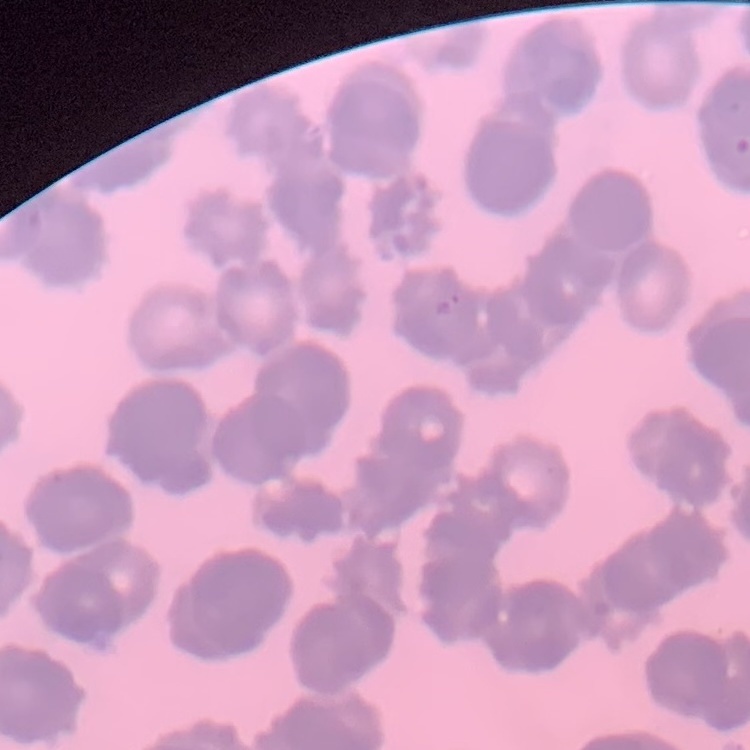

The red blood cells show rouleaux formation. Stained with either Field's or Giemsa. One tile cut from a larger photomicrograph. Thin peripheral smear.